Classify this cell by malaria status.
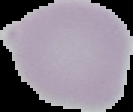
Uninfected.

image_size: 133×112 pixels
image_type: segmented cell region on a black background
preparation: thin blood film